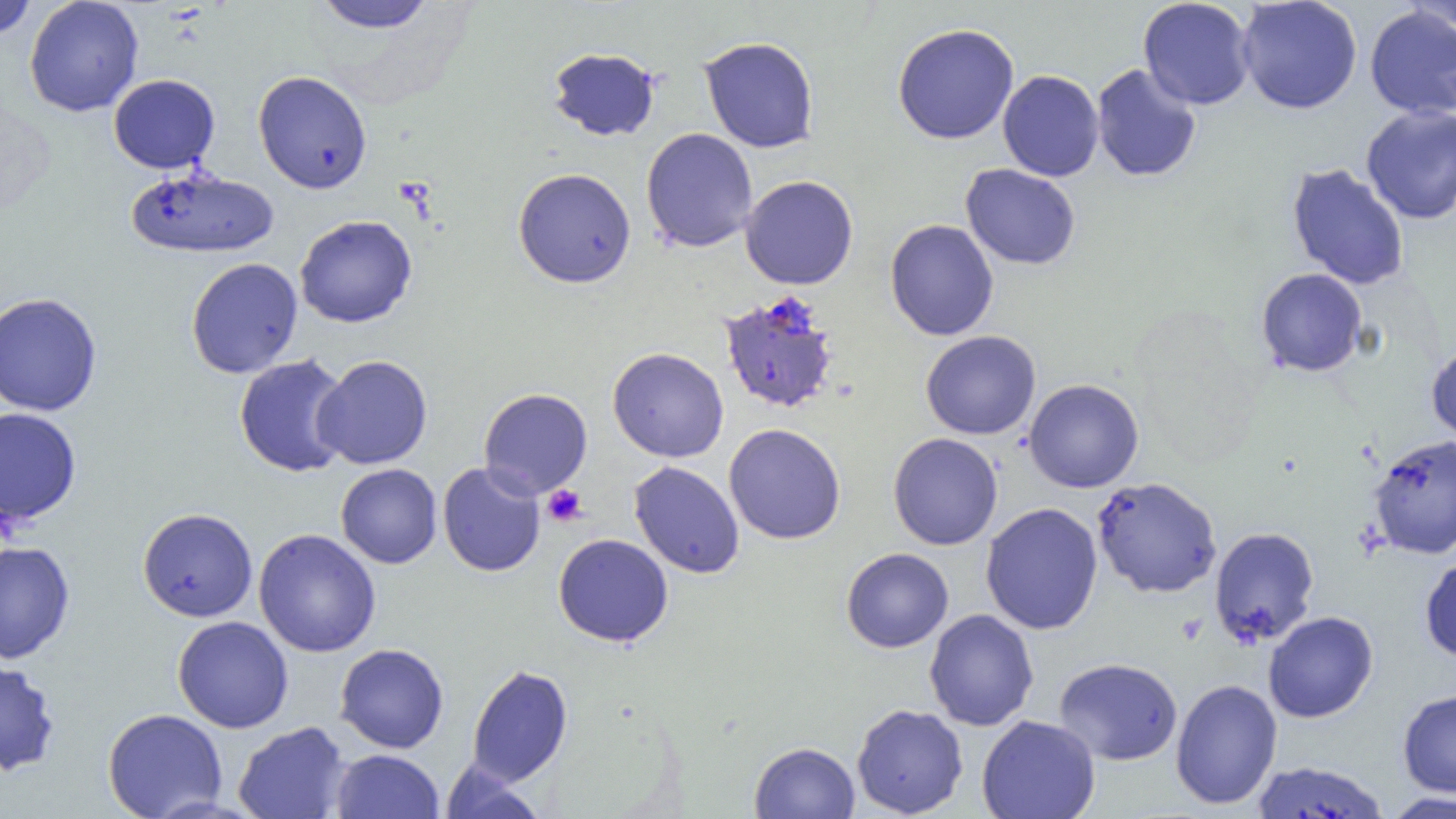
slide-level diagnosis = Plasmodium falciparum
preparation = thin blood film
modality = light microscopy
magnification = 1000x
uninfected red blood cell locations = approximate bounding boxes as [x1, y1, x2, y2] in pixels: [0, 0, 37, 40], [24, 0, 144, 117], [311, 0, 440, 33], [1138, 0, 1255, 110], [1236, 0, 1362, 114], [1401, 0, 1456, 36], [1364, 5, 1456, 119], [892, 22, 1019, 144], [699, 36, 820, 153], [548, 47, 661, 141], [1090, 64, 1202, 183], [253, 70, 372, 194], [997, 70, 1104, 181], [108, 74, 220, 173], [1361, 105, 1456, 224], [641, 127, 758, 252], [960, 163, 1081, 270], [1286, 163, 1410, 292], [125, 166, 278, 259], [513, 168, 636, 288], [740, 175, 858, 290], [294, 215, 417, 328], [884, 219, 999, 341], [186, 257, 303, 379], [1256, 268, 1368, 377], [0, 292, 103, 416], [920, 330, 1040, 440], [1426, 342, 1456, 445], [607, 347, 729, 462], [234, 354, 353, 478], [313, 355, 432, 470], [1023, 378, 1144, 493], [478, 387, 593, 499], [0, 407, 81, 526], [724, 423, 846, 544], [887, 432, 1003, 550], [1367, 434, 1456, 559], [629, 461, 745, 579], [437, 462, 545, 577], [336, 463, 442, 568], [1091, 476, 1222, 599], [980, 502, 1103, 635], [137, 507, 258, 622], [1209, 526, 1320, 648], [254, 528, 381, 657], [553, 533, 674, 647], [0, 541, 75, 664], [840, 548, 954, 653], [1420, 555, 1456, 662], [924, 609, 1039, 731], [1263, 611, 1378, 723], [172, 615, 294, 733], [334, 643, 449, 753], [1054, 657, 1183, 765], [0, 661, 61, 776], [466, 663, 573, 786], [1170, 678, 1283, 810], [1397, 689, 1456, 797], [851, 703, 968, 818], [102, 708, 228, 819], [977, 714, 1100, 819], [233, 721, 350, 819], [749, 742, 860, 818], [331, 749, 444, 819], [439, 761, 545, 819], [1250, 761, 1390, 819], [1382, 791, 1456, 818]
platelet locations = approximate bounding boxes as [x1, y1, x2, y2] in pixels: [541, 484, 587, 527]
Plasmodium falciparum-infected red blood cell locations = approximate bounding boxes as [x1, y1, x2, y2] in pixels: [719, 291, 841, 414]
image size = 1456×819 pixels
field of view = single